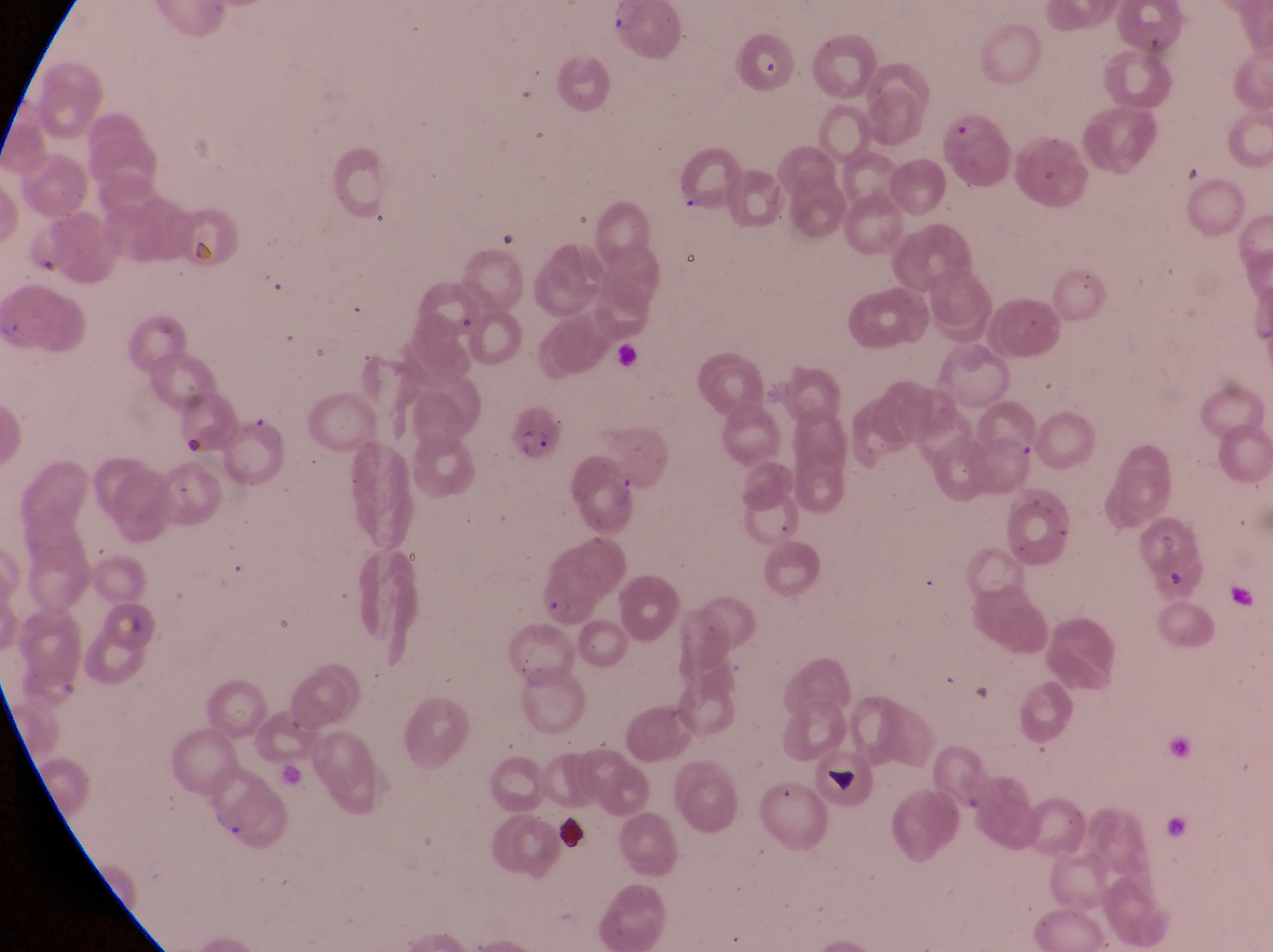

Approximate bounding boxes as [left, top, right, bottom] in pixels. Artifact (platelet-like body, stain precipitate, or debris) locations: [752, 50, 785, 87], [821, 749, 871, 802], [552, 811, 592, 858]. Parasitised red blood cell locations: [941, 118, 1015, 200], [507, 397, 565, 465], [532, 565, 597, 623]. Thin blood smear. Photographed through the eyepiece of an Olympus CX-23 microscope with a smartphone camera. Sample from Uganda. Image is 1273×952 pixels. Single field of view. Magnification of 1000x.